Comment on the morphology of the erythrocytes.
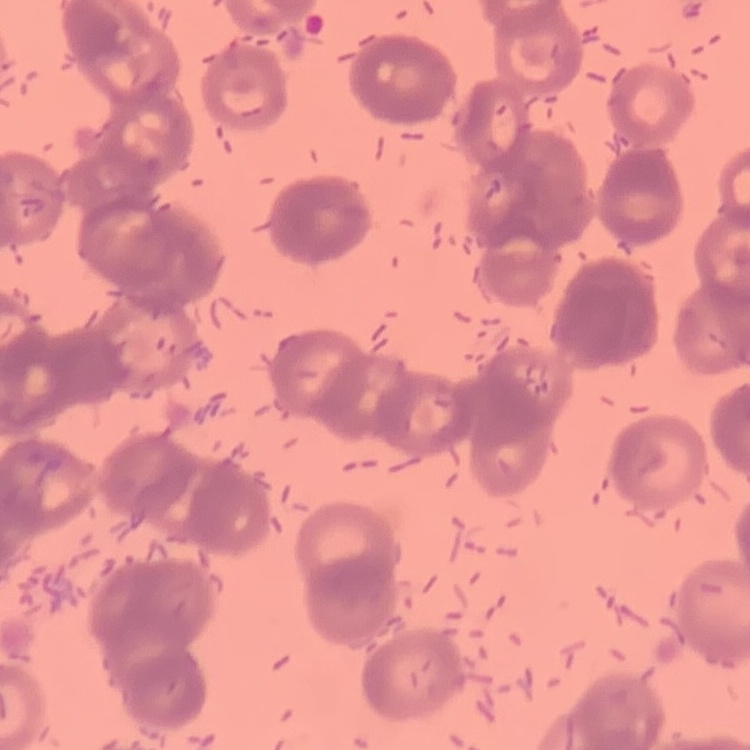
Rouleaux formation.

Summary:
  - Preparation: thin blood film
  - Image type: one tile cut from a larger photomicrograph
  - Stain: Field's or Giemsa